Name the blood parasite species.
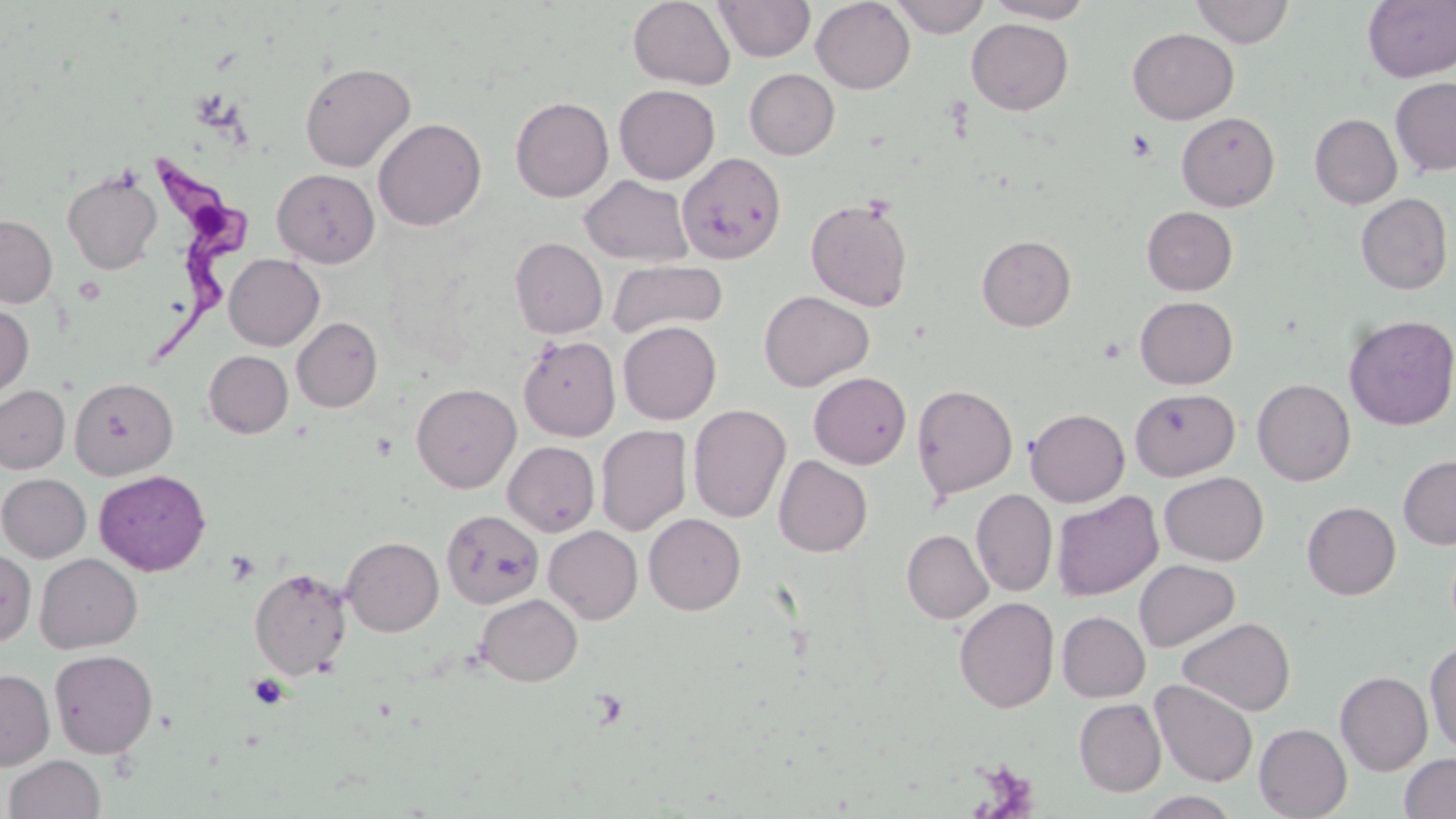

Trypanosoma brucei.

preparation = thin blood smear
Trypanosoma brucei locations = approximate bounding boxes as [x1, y1, x2, y2] in pixels: [149, 153, 249, 359]
magnification = 1000x
field of view = single
stain = May-Grünwald-Giemsa
image size = 1456×819 pixels
modality = optical microscopy
uninfected red blood cell locations = approximate bounding boxes as [x1, y1, x2, y2] in pixels: [628, 0, 735, 90], [714, 0, 815, 62], [811, 0, 915, 93], [889, 0, 990, 38], [983, 0, 1097, 23], [1190, 0, 1295, 47], [1362, 1, 1456, 82], [966, 18, 1073, 115], [1127, 28, 1239, 124], [299, 61, 415, 172], [744, 68, 840, 159], [1390, 77, 1456, 176], [614, 84, 720, 184], [510, 96, 614, 202], [1176, 112, 1279, 211], [1309, 114, 1402, 209], [373, 118, 486, 231], [677, 152, 787, 265], [272, 168, 379, 267], [63, 170, 162, 274], [580, 176, 693, 266], [1355, 193, 1453, 294], [805, 196, 914, 312], [1142, 206, 1237, 295], [0, 214, 57, 307], [977, 235, 1076, 331], [510, 237, 607, 338], [510, 245, 723, 339], [224, 254, 324, 350], [607, 259, 728, 341], [758, 290, 874, 391], [1134, 296, 1238, 389], [0, 303, 33, 400], [1343, 315, 1456, 430], [292, 317, 382, 412], [618, 321, 721, 424], [519, 335, 620, 442], [204, 350, 293, 438], [808, 372, 911, 469], [69, 377, 178, 480], [809, 379, 1017, 481], [1252, 379, 1356, 485], [411, 383, 521, 493], [912, 383, 1018, 500], [0, 385, 69, 474], [1130, 388, 1239, 480], [688, 404, 791, 523], [1025, 408, 1130, 506], [595, 425, 691, 535], [503, 441, 599, 536], [1398, 454, 1456, 549], [773, 455, 873, 557], [94, 470, 211, 575], [1159, 471, 1269, 566], [0, 473, 91, 562], [971, 489, 1057, 597], [1052, 491, 1163, 601], [1302, 502, 1401, 599], [442, 509, 543, 608], [644, 513, 746, 615], [544, 526, 642, 624], [901, 529, 993, 624], [342, 536, 443, 636], [0, 550, 36, 644], [35, 553, 142, 653], [1134, 559, 1240, 652], [249, 566, 352, 679], [476, 594, 582, 686], [953, 597, 1059, 713], [1056, 611, 1150, 702], [1177, 617, 1295, 716], [1425, 640, 1456, 754], [49, 649, 158, 758], [0, 669, 55, 770], [1335, 671, 1433, 775], [1150, 679, 1258, 787], [1074, 698, 1166, 796], [1254, 723, 1352, 819], [1399, 753, 1456, 818], [4, 755, 106, 819], [1138, 791, 1242, 818]
platelet locations = approximate bounding boxes as [x1, y1, x2, y2] in pixels: [1127, 129, 1157, 162], [226, 551, 260, 585], [248, 673, 289, 710], [588, 688, 630, 731], [972, 759, 1039, 816]